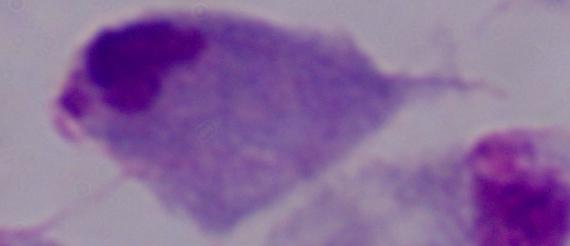
magnification = 1000x
modality = micrograph
identification = trichomonad